State which parasite is depicted.
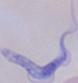

A trypanosome.

Summary:
  - Modality: photomicrograph
  - Magnification: 1000x